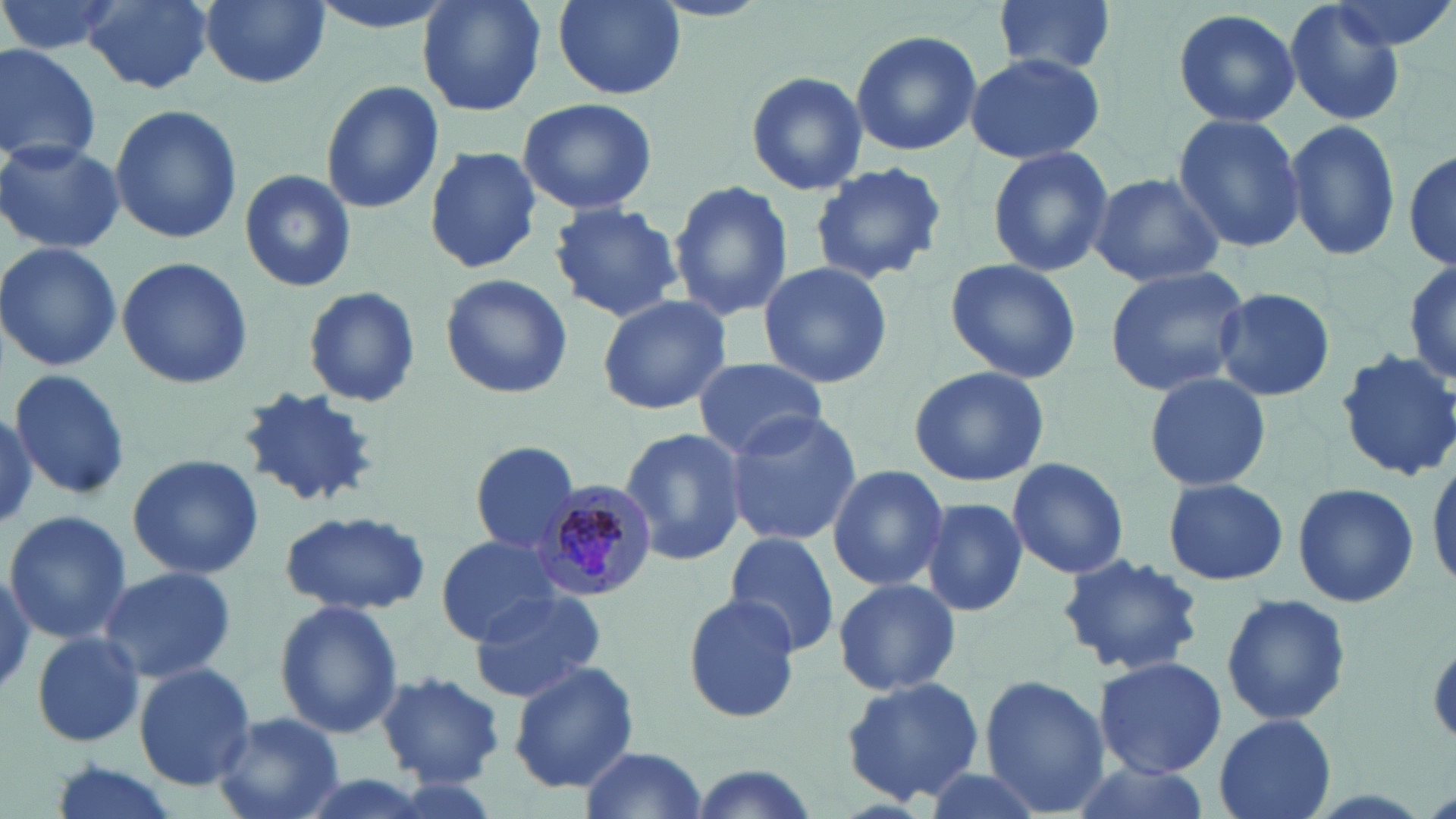 Approximate bounding boxes as [x1, y1, x2, y2] in pixels. Plasmodium malariae-infected red blood cell locations: [541, 478, 658, 600]. Uninfected red blood cell locations: [1, 0, 124, 58], [80, 0, 219, 94], [198, 0, 330, 89], [416, 0, 548, 116], [551, 0, 687, 101], [990, 0, 1122, 80], [1281, 0, 1407, 126], [1331, 0, 1456, 53], [1171, 6, 1301, 129], [849, 29, 983, 157], [0, 43, 102, 168], [966, 53, 1105, 165], [744, 69, 869, 196], [319, 80, 444, 215], [517, 96, 658, 215], [110, 103, 242, 243], [1171, 115, 1307, 253], [1284, 119, 1403, 264], [0, 138, 124, 256], [985, 143, 1113, 278], [424, 145, 544, 274], [1404, 147, 1456, 273], [808, 162, 948, 285], [238, 169, 357, 292], [1088, 171, 1227, 288], [670, 179, 794, 322], [547, 200, 683, 321], [0, 242, 122, 372], [115, 257, 254, 391], [943, 257, 1082, 384], [1404, 260, 1456, 388], [758, 261, 894, 389], [1102, 266, 1250, 396], [438, 274, 573, 399], [301, 285, 422, 408], [1210, 286, 1336, 402], [594, 295, 732, 417], [1336, 349, 1456, 482], [691, 356, 827, 457], [908, 363, 1049, 487], [9, 367, 132, 500], [1142, 371, 1272, 494], [238, 386, 381, 508], [0, 408, 37, 527], [723, 410, 863, 545], [619, 423, 746, 566], [468, 440, 583, 556], [126, 454, 264, 578], [1426, 455, 1456, 594], [1006, 457, 1130, 579], [826, 463, 950, 592], [1159, 477, 1291, 585], [1292, 480, 1419, 608], [917, 497, 1029, 618], [3, 508, 132, 644], [279, 508, 433, 616], [722, 533, 840, 656], [432, 534, 567, 646], [1058, 553, 1203, 677], [97, 566, 236, 682], [0, 568, 35, 697], [831, 577, 962, 698], [467, 589, 610, 702], [681, 593, 804, 722], [1220, 593, 1351, 725], [272, 599, 404, 738], [30, 632, 145, 748], [1093, 655, 1227, 777], [507, 659, 640, 793], [133, 662, 256, 791], [375, 670, 506, 787], [977, 675, 1108, 816], [841, 676, 986, 806], [213, 711, 346, 819], [1212, 713, 1337, 819], [579, 745, 708, 819], [1062, 758, 1211, 819], [47, 762, 180, 819], [912, 763, 1055, 819], [685, 764, 825, 819]. Slide-level diagnosis: Plasmodium malariae. Image is 1456×819 pixels. May-Grünwald-Giemsa stain. Captured at 1000x magnification. Light microscopy. Thin blood film. Single field of view.